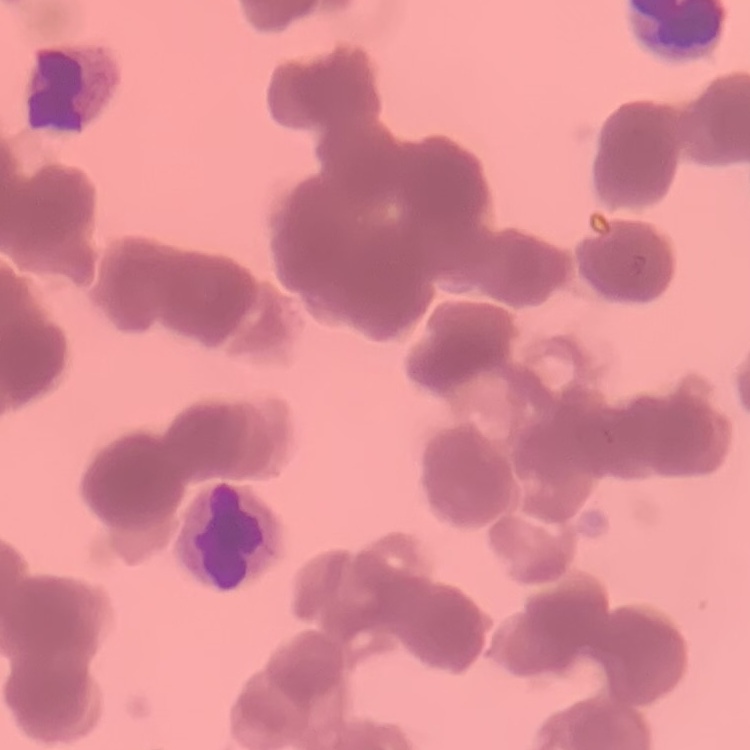

Summary:
  - Erythrocyte morphology: rouleaux formation
  - Preparation: thin blood smear
  - Image type: one tile cut from a larger photomicrograph
  - Stain: Field's or Giemsa